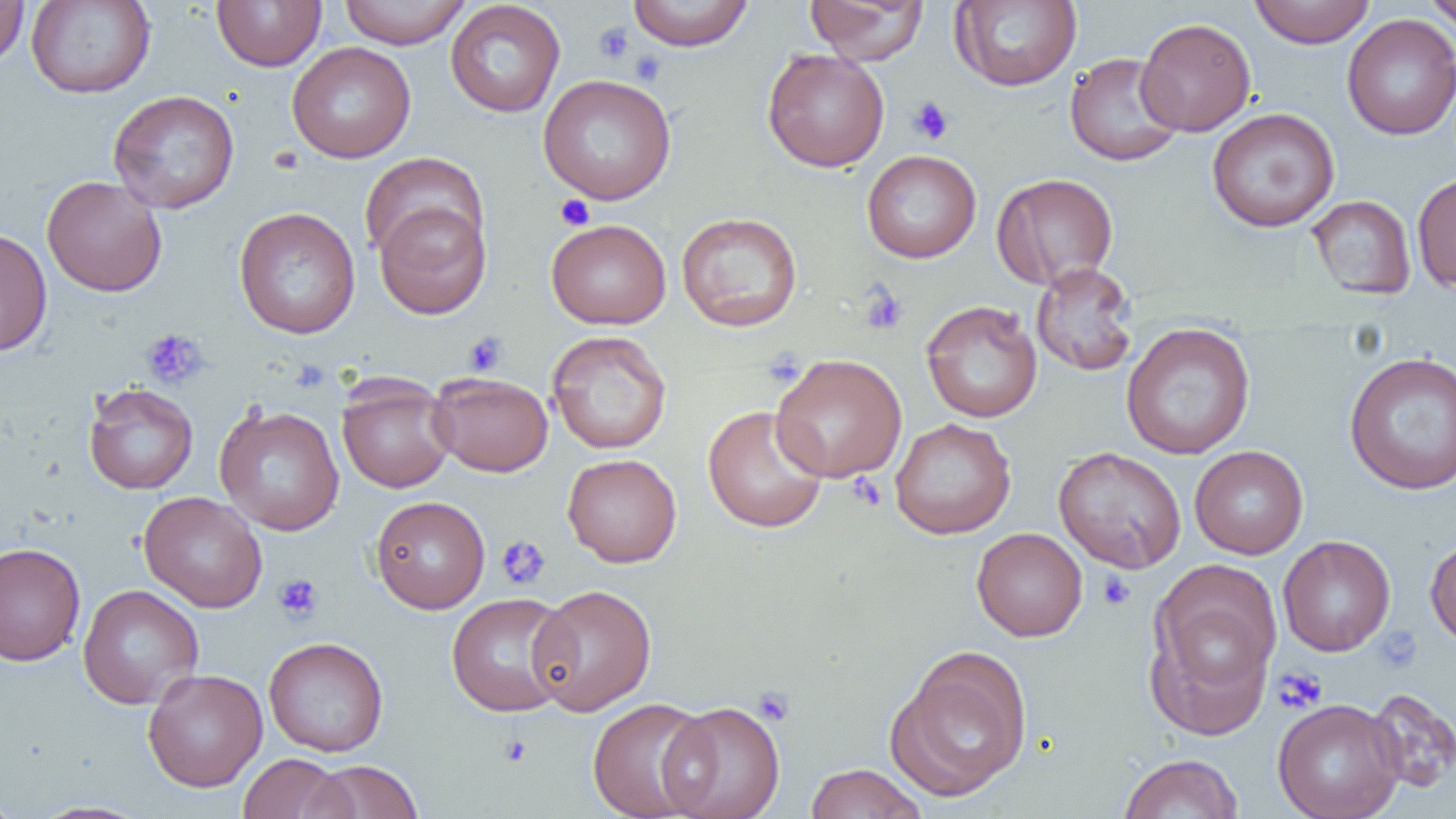
slide-level diagnosis = no evidence of blood parasites
magnification = 1000x
uninfected red blood cell locations = approximate bounding boxes as [x1, y1, x2, y2] in pixels: [0, 0, 29, 66], [25, 0, 155, 98], [212, 0, 326, 71], [338, 0, 472, 49], [626, 0, 754, 50], [805, 0, 929, 64], [950, 0, 1082, 91], [1249, 0, 1376, 48], [1421, 0, 1456, 32], [445, 1, 566, 118], [1342, 14, 1456, 141], [1136, 17, 1256, 136], [286, 42, 416, 163], [762, 48, 890, 172], [1064, 52, 1185, 167], [537, 73, 677, 205], [107, 89, 240, 214], [1206, 107, 1340, 232], [862, 150, 981, 263], [359, 152, 488, 263], [991, 172, 1118, 290], [1411, 172, 1456, 293], [41, 176, 167, 297], [1306, 195, 1417, 300], [374, 200, 492, 319], [233, 207, 361, 339], [676, 211, 803, 332], [546, 219, 671, 329], [0, 227, 52, 357], [1031, 262, 1139, 377], [921, 300, 1042, 423], [1120, 322, 1256, 460], [547, 330, 672, 454], [1343, 351, 1456, 495], [770, 353, 907, 482], [428, 372, 554, 477], [337, 378, 455, 493], [83, 383, 198, 494], [214, 403, 345, 536], [703, 405, 829, 533], [890, 418, 1016, 539], [1189, 445, 1308, 559], [1053, 446, 1187, 573], [562, 453, 682, 567], [139, 491, 267, 613], [370, 495, 490, 613], [971, 527, 1088, 642], [1425, 533, 1456, 649], [1278, 535, 1395, 656], [0, 541, 86, 666], [1146, 573, 1277, 730], [77, 584, 204, 709], [528, 584, 656, 716], [446, 592, 576, 717], [263, 636, 389, 757], [886, 647, 1033, 802], [143, 668, 268, 792], [1366, 687, 1456, 793], [585, 696, 717, 819], [1272, 698, 1405, 819], [659, 701, 785, 819], [238, 753, 349, 819], [1118, 753, 1243, 819], [303, 760, 424, 818], [804, 763, 927, 819], [0, 785, 21, 819], [30, 801, 151, 819]
preparation = thin blood film
field of view = single
image size = 1456×819 pixels
platelet locations = approximate bounding boxes as [x1, y1, x2, y2] in pixels: [593, 23, 635, 65], [629, 50, 667, 86], [907, 96, 954, 145], [555, 195, 596, 231], [860, 285, 908, 335], [140, 328, 209, 390], [462, 332, 508, 377], [846, 472, 886, 510], [496, 535, 551, 590], [1096, 570, 1136, 611], [273, 573, 324, 623], [1373, 627, 1422, 671], [1273, 667, 1327, 713], [752, 686, 795, 725], [499, 734, 533, 766]
modality = light microscopy